Report the malaria status of this cell.
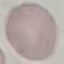
Uninfected.

Giemsa-stained preparation. Cell patch, automatically extracted from a larger field of view and resized to 64 × 64 pixels. Thin blood film. Photographed with a smartphone camera at the microscope eyepiece.